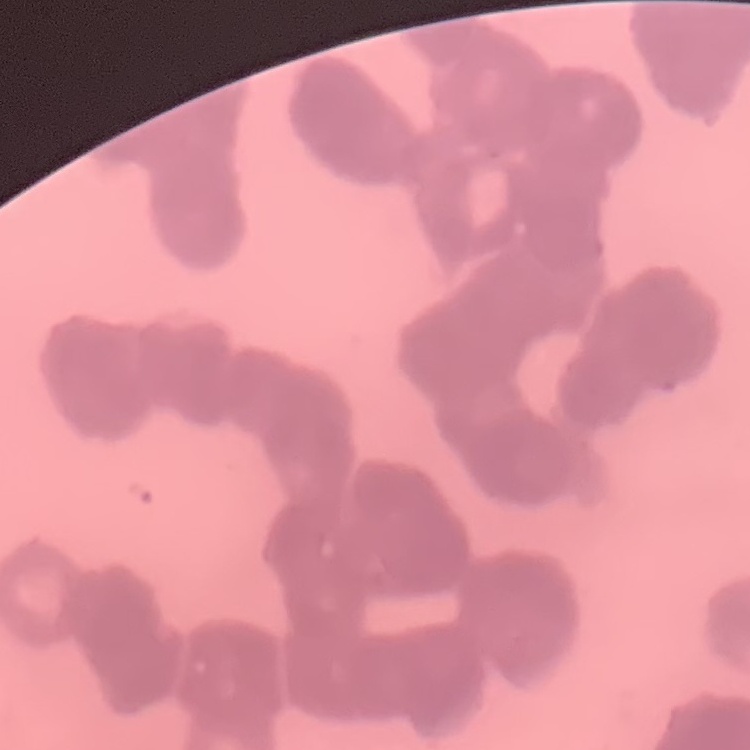

Summary:
  - Red blood cell morphology: rouleaux formation
  - Image type: square crop of a larger photomicrograph
  - Preparation: thin blood smear
  - Stain: Field's or Giemsa